Classify this cell by malaria status.
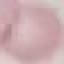
Uninfected.

Summary:
  - Preparation: thin blood film
  - Stain: Giemsa
  - Capture: smartphone camera at the microscope eyepiece
  - Image type: cell patch, automatically extracted from a larger field of view and resized to 64 × 64 pixels